Identify the parasite.
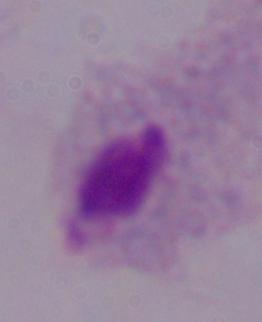

This is a trichomonad.

1000x magnification. Photomicrograph.